Report the malaria status of this cell.
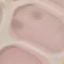

It is uninfected.

{
  "preparation": "thin blood film",
  "image_type": "cell patch, automatically extracted from a larger field of view and resized to 64 × 64 pixels",
  "capture": "smartphone camera at the microscope eyepiece",
  "stain": "Giemsa"
}